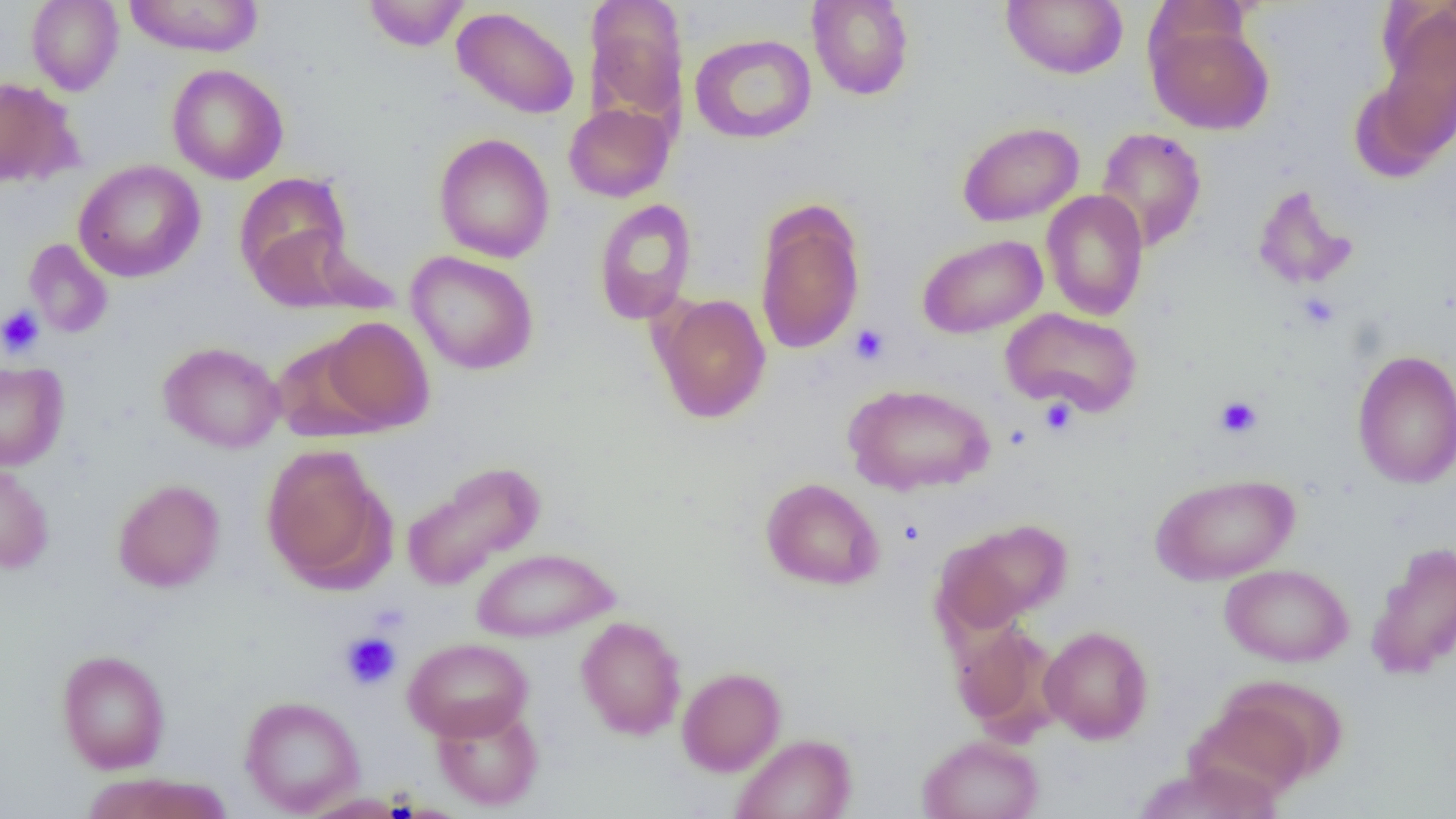
slide-level diagnosis = negative for blood parasites
magnification = 1000x
preparation = thin blood smear
image size = 1456×819 pixels
modality = light microscopy
uninfected red blood cell locations = approximate bounding boxes as named x1/y1/x2/y2 corners in pixels: (x1=25, y1=0, x2=124, y2=95), (x1=123, y1=0, x2=264, y2=57), (x1=362, y1=0, x2=470, y2=52), (x1=807, y1=0, x2=914, y2=101), (x1=1001, y1=0, x2=1128, y2=79), (x1=1374, y1=1, x2=1456, y2=151), (x1=585, y1=2, x2=689, y2=125), (x1=451, y1=6, x2=580, y2=119), (x1=1146, y1=18, x2=1275, y2=134), (x1=689, y1=33, x2=817, y2=144), (x1=167, y1=63, x2=289, y2=184), (x1=0, y1=77, x2=76, y2=188), (x1=563, y1=102, x2=674, y2=202), (x1=957, y1=121, x2=1084, y2=226), (x1=1094, y1=127, x2=1207, y2=252), (x1=433, y1=133, x2=555, y2=263), (x1=73, y1=160, x2=206, y2=283), (x1=234, y1=172, x2=354, y2=300), (x1=1251, y1=184, x2=1358, y2=291), (x1=1041, y1=190, x2=1149, y2=321), (x1=592, y1=198, x2=698, y2=326), (x1=753, y1=200, x2=866, y2=355), (x1=916, y1=234, x2=1047, y2=338), (x1=23, y1=238, x2=114, y2=339), (x1=406, y1=250, x2=539, y2=375), (x1=651, y1=292, x2=772, y2=424), (x1=1000, y1=307, x2=1143, y2=417), (x1=319, y1=316, x2=435, y2=434), (x1=271, y1=337, x2=384, y2=441), (x1=158, y1=341, x2=285, y2=453), (x1=1352, y1=349, x2=1456, y2=489), (x1=0, y1=360, x2=69, y2=471), (x1=844, y1=382, x2=995, y2=496), (x1=261, y1=445, x2=393, y2=590), (x1=0, y1=460, x2=54, y2=574), (x1=401, y1=460, x2=546, y2=590), (x1=1150, y1=472, x2=1300, y2=585), (x1=760, y1=477, x2=884, y2=591), (x1=112, y1=479, x2=225, y2=593), (x1=937, y1=519, x2=1071, y2=633), (x1=1366, y1=541, x2=1456, y2=681), (x1=471, y1=547, x2=618, y2=642), (x1=1219, y1=563, x2=1353, y2=667), (x1=575, y1=616, x2=687, y2=740), (x1=950, y1=618, x2=1057, y2=736), (x1=1039, y1=625, x2=1154, y2=744), (x1=403, y1=637, x2=533, y2=742), (x1=56, y1=650, x2=170, y2=773), (x1=676, y1=667, x2=786, y2=776), (x1=1198, y1=677, x2=1345, y2=796), (x1=240, y1=695, x2=365, y2=816), (x1=432, y1=702, x2=544, y2=811), (x1=730, y1=733, x2=857, y2=819), (x1=917, y1=734, x2=1044, y2=819), (x1=1133, y1=762, x2=1283, y2=819), (x1=80, y1=772, x2=234, y2=819), (x1=297, y1=792, x2=411, y2=818)
field of view = one of a larger specimen
platelet locations = approximate bounding boxes as named x1/y1/x2/y2 corners in pixels: (x1=0, y1=304, x2=45, y2=358), (x1=849, y1=324, x2=891, y2=365), (x1=1214, y1=396, x2=1262, y2=439), (x1=1039, y1=398, x2=1078, y2=436), (x1=339, y1=631, x2=402, y2=690)